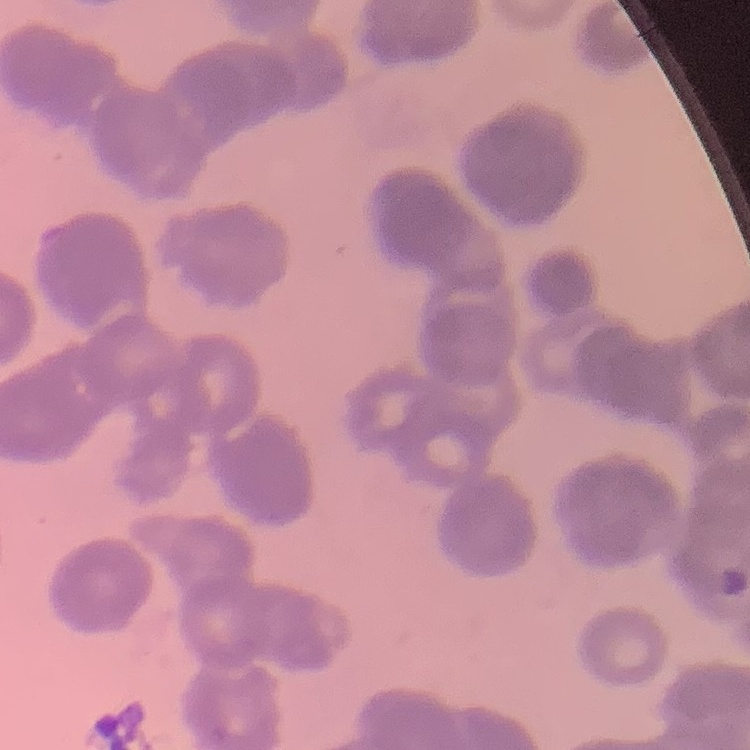

Summary:
  - Erythrocyte morphology: rouleaux formation
  - Stain: Field's or Giemsa
  - Image type: one tile cut from a larger photomicrograph
  - Preparation: thin blood film